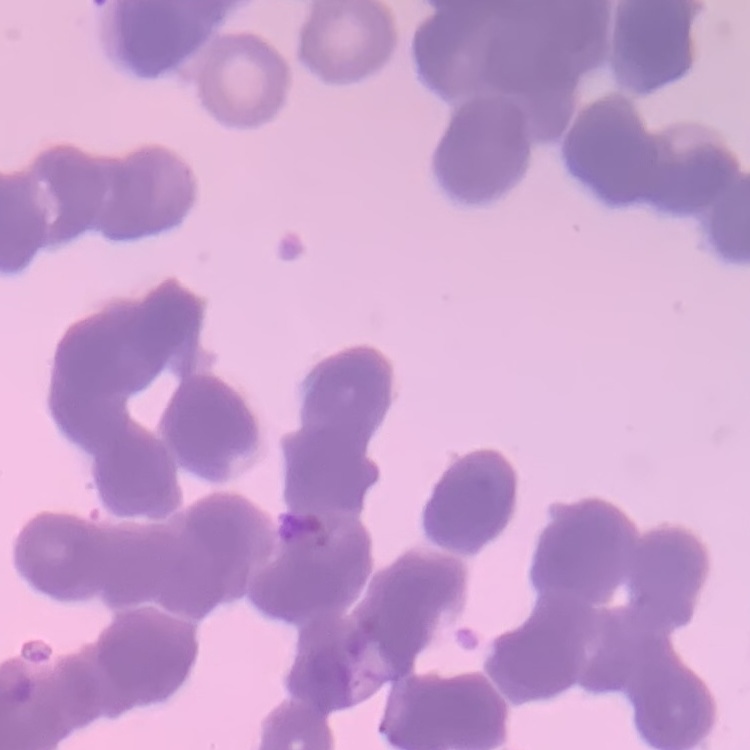

Summary:
  - Erythrocyte morphology: rouleaux formation
  - Image type: square crop of a larger photomicrograph
  - Preparation: thin blood film
  - Stain: Field's or Giemsa